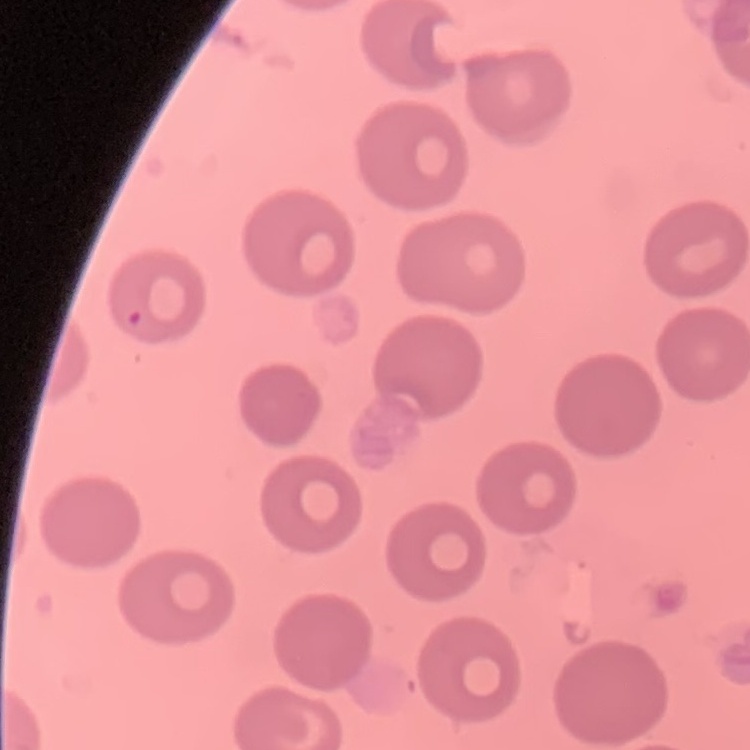

{
  "erythrocyte_morphology": "no rouleaux formation",
  "stain": "Field's or Giemsa",
  "preparation": "thin blood smear",
  "image_type": "square crop of a larger photomicrograph"
}